Locate every Babesia divergens-infected red blood cell.
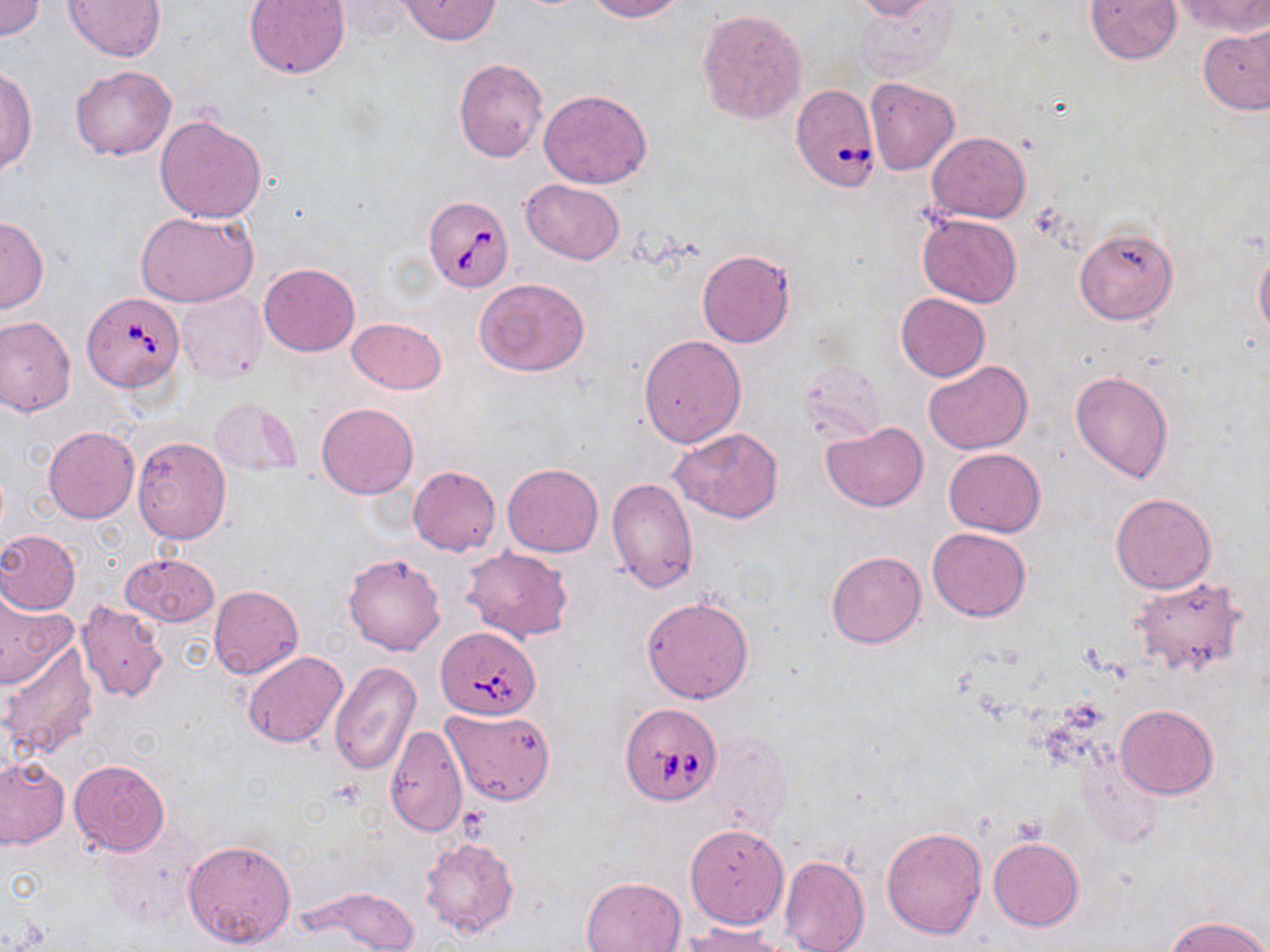
Approximate bounding boxes as (x1,y1)-(x2,y2) corner pairs in pixels.
Babesia divergens-infected red blood cells: (790,83)-(881,191), (424,197)-(513,291), (82,292)-(184,391), (435,627)-(539,720), (620,703)-(723,806).

Uninfected red blood cell locations: (244,0)-(349,79), (399,0)-(500,45), (587,0)-(682,22), (851,0)-(943,21), (1085,0)-(1182,65), (1175,0)-(1268,35), (1,1)-(44,41), (63,1)-(166,61), (854,4)-(959,76), (696,8)-(807,124), (1198,25)-(1270,114), (453,57)-(549,163), (1,65)-(37,177), (70,65)-(176,161), (865,76)-(959,175), (538,89)-(652,188), (155,114)-(269,223), (927,132)-(1030,223), (522,179)-(625,264), (136,210)-(259,307), (916,211)-(1021,307), (0,216)-(47,313), (1074,227)-(1177,326), (1254,245)-(1270,342), (697,248)-(796,348), (259,262)-(360,356), (475,277)-(590,378), (175,290)-(267,383), (895,293)-(990,382), (0,316)-(75,416), (347,317)-(447,393), (638,334)-(747,448), (923,360)-(1033,454), (803,364)-(883,439), (1070,369)-(1174,482), (209,398)-(303,477), (316,402)-(420,500), (820,421)-(927,512), (43,426)-(139,523), (668,428)-(783,521), (132,436)-(232,542), (943,448)-(1046,537), (503,463)-(603,557), (407,466)-(501,556), (607,476)-(699,592), (1110,492)-(1216,595), (928,528)-(1031,622), (0,530)-(81,614), (462,547)-(572,643), (826,551)-(926,648), (121,552)-(220,628), (342,552)-(445,655), (1130,576)-(1250,680), (209,585)-(304,678), (0,591)-(78,692), (642,596)-(753,704), (76,600)-(169,703), (1,641)-(98,763), (241,651)-(348,750), (328,661)-(421,777), (1116,704)-(1218,798), (442,708)-(555,804), (385,724)-(467,836), (706,732)-(792,835), (0,756)-(69,849), (68,758)-(170,855), (684,823)-(788,930), (98,824)-(202,929), (881,827)-(986,939), (419,836)-(520,937), (988,837)-(1085,932), (183,838)-(297,950), (779,854)-(870,952), (580,877)-(686,952), (302,887)-(420,950), (1165,915)-(1270,952), (680,923)-(796,952). Slide-level diagnosis: Babesia divergens. May-Grünwald-Giemsa stain. Thin blood film. Image is 1270×952 pixels. Optical microscopy. Single field of view. 1000x magnification.